Classify this cell by malaria status.
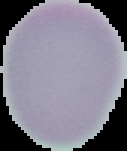
It is uninfected.

Summary:
  - Image size: 127×151 pixels
  - Image type: segmented cell region on a black background
  - Preparation: thin blood smear